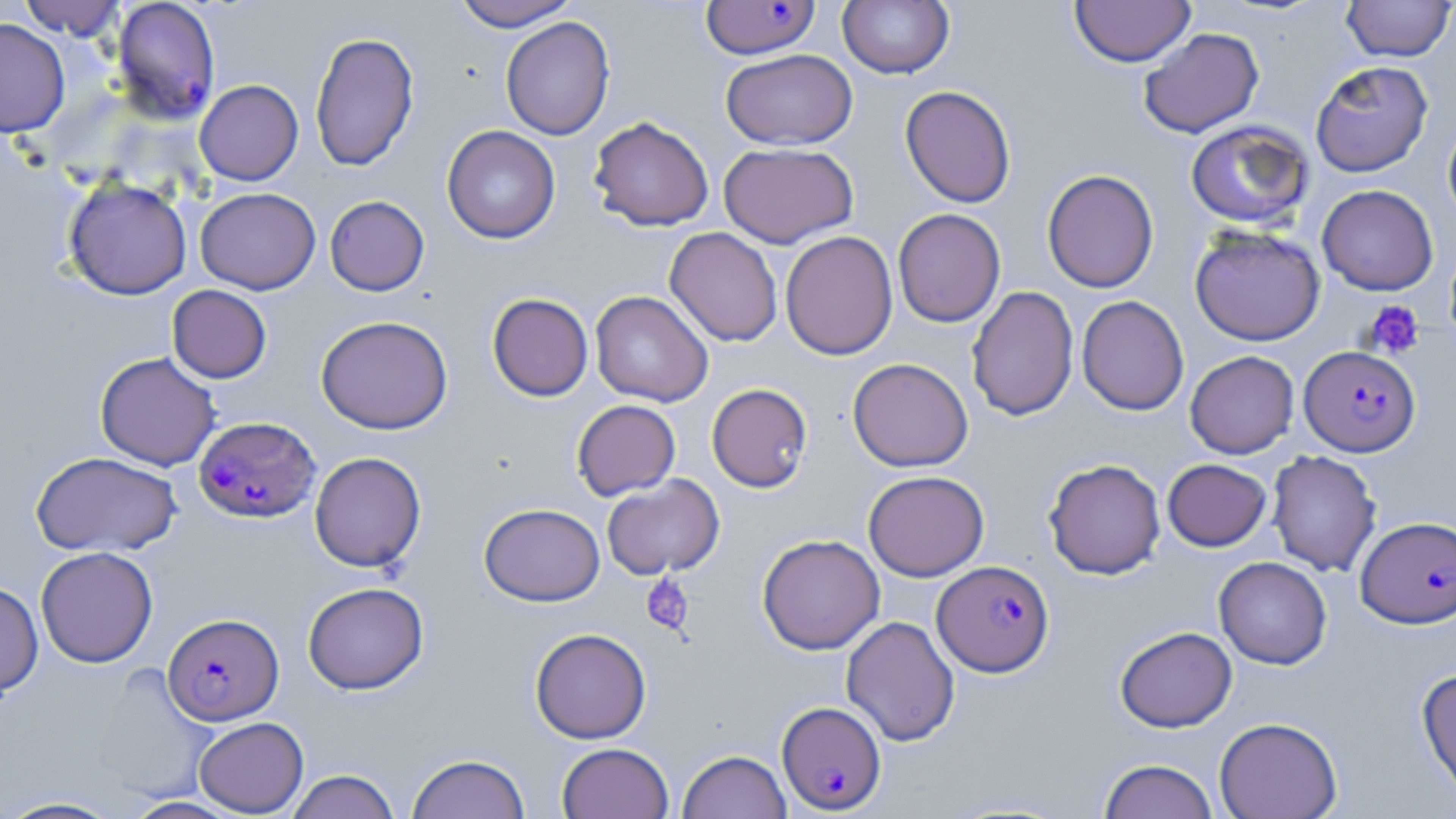
slide-level diagnosis = Plasmodium falciparum
stain = May-Grünwald-Giemsa
field of view = one of a larger specimen
preparation = thin blood film
Plasmodium falciparum-infected red blood cell locations = approximate bounding boxes as (x1,y1)-(x2,y2) corner pairs in pixels: (111,1)-(221,125), (700,1)-(820,60), (1299,345)-(1420,457), (194,416)-(320,522), (1355,516)-(1456,628), (932,560)-(1054,677), (163,612)-(284,725), (777,700)-(887,814)
image size = 1456×819 pixels
uninfected red blood cell locations = approximate bounding boxes as (x1,y1)-(x2,y2) corner pairs in pixels: (17,0)-(127,40), (450,0)-(579,31), (837,0)-(955,79), (1341,0)-(1455,62), (1069,1)-(1196,67), (500,16)-(615,140), (0,18)-(70,138), (1138,27)-(1265,138), (310,30)-(419,172), (720,49)-(858,150), (1310,60)-(1433,177), (192,75)-(301,181), (900,85)-(1016,208), (588,116)-(714,232), (1442,118)-(1456,226), (1185,120)-(1314,230), (442,125)-(561,244), (718,142)-(859,247), (1042,168)-(1159,293), (63,177)-(192,300), (1317,184)-(1438,295), (195,187)-(321,295), (324,195)-(429,296), (893,208)-(1006,327), (1189,225)-(1325,346), (664,227)-(783,347), (779,230)-(898,360), (167,285)-(272,383), (966,285)-(1079,421), (590,290)-(713,407), (487,293)-(593,401), (1077,295)-(1189,415), (315,315)-(453,434), (1185,350)-(1299,459), (95,352)-(221,471), (848,357)-(973,472), (707,383)-(812,493), (571,399)-(681,501), (30,450)-(181,557), (1267,450)-(1382,577), (309,451)-(426,572), (1043,458)-(1166,579), (1163,458)-(1271,551), (863,470)-(989,581), (601,475)-(725,580), (479,503)-(605,606), (757,533)-(885,655), (35,546)-(158,668), (1213,556)-(1332,669), (0,581)-(43,697), (303,581)-(429,694), (841,615)-(960,747), (1115,626)-(1237,732), (530,628)-(651,743), (91,663)-(216,804), (1416,666)-(1456,805), (194,716)-(309,817), (1214,717)-(1343,819), (556,742)-(674,819), (677,749)-(791,819), (407,753)-(531,819), (1098,758)-(1219,819), (285,770)-(401,819), (0,795)-(127,818), (122,796)-(244,818)
modality = light microscopy
platelet locations = approximate bounding boxes as (x1,y1)-(x2,y2) corner pairs in pixels: (1362,300)-(1424,359), (642,574)-(693,636)
magnification = 1000x